Locate and identify every blood parasite.
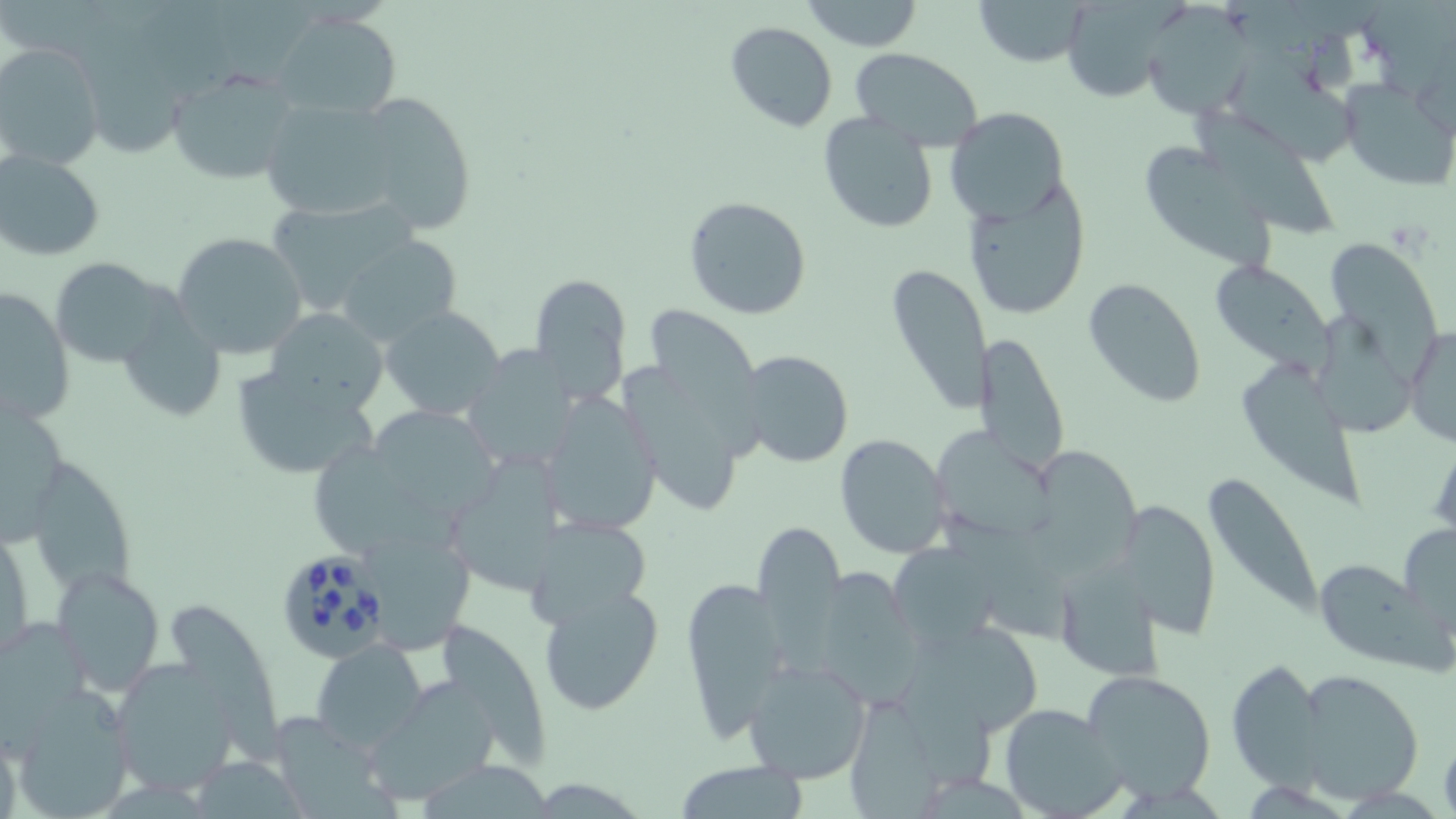
Approximate bounding boxes as (x1, y1, x2, y2) in pixels.
Babesia divergens-infected red blood cells: (281, 545, 401, 661).
No Plasmodium falciparum, Plasmodium ovale, Plasmodium malariae, Plasmodium vivax, or Trypanosoma brucei observed.

Uninfected red blood cell locations: (802, 0, 923, 52), (972, 0, 1090, 68), (1056, 0, 1181, 104), (1142, 10, 1245, 118), (272, 12, 401, 120), (724, 21, 839, 133), (0, 41, 106, 169), (848, 48, 985, 152), (1223, 54, 1359, 172), (167, 70, 301, 188), (1341, 82, 1452, 187), (352, 92, 478, 235), (259, 97, 403, 219), (946, 107, 1068, 225), (818, 111, 938, 233), (1194, 111, 1343, 242), (1145, 146, 1277, 277), (0, 148, 104, 260), (962, 181, 1094, 319), (684, 195, 814, 321), (172, 231, 309, 358), (334, 234, 463, 345), (1326, 241, 1444, 390), (49, 258, 181, 369), (1207, 260, 1332, 371), (884, 261, 994, 415), (529, 273, 633, 405), (1083, 277, 1207, 408), (126, 279, 226, 423), (1, 285, 75, 426), (645, 305, 764, 410), (380, 306, 507, 419), (261, 307, 389, 420), (1316, 317, 1421, 449), (1404, 323, 1456, 447), (977, 332, 1070, 476), (459, 347, 586, 472), (735, 349, 855, 468), (617, 359, 754, 520), (1243, 362, 1365, 512), (228, 364, 378, 480), (539, 390, 662, 535), (0, 401, 67, 562), (368, 412, 515, 534), (930, 429, 1069, 544), (833, 433, 953, 559), (312, 437, 434, 558), (1025, 447, 1156, 583), (447, 452, 567, 595), (40, 464, 142, 617), (1198, 469, 1324, 620), (1116, 497, 1221, 639), (523, 514, 657, 635), (753, 520, 848, 663), (1399, 520, 1456, 634), (367, 530, 481, 655), (887, 542, 999, 653), (1049, 555, 1166, 677), (1310, 562, 1437, 668), (53, 566, 165, 697), (818, 568, 945, 716), (676, 572, 787, 740), (537, 585, 665, 717), (167, 603, 289, 778), (430, 616, 555, 768), (907, 617, 1046, 737), (0, 619, 94, 740), (312, 639, 427, 751), (1226, 656, 1328, 791), (743, 659, 873, 785), (108, 661, 239, 797), (1293, 667, 1424, 804), (1081, 668, 1218, 800), (358, 678, 501, 806), (9, 686, 136, 817), (838, 691, 964, 816), (996, 702, 1128, 819), (268, 712, 398, 819), (1440, 733, 1456, 819), (184, 757, 312, 816), (413, 760, 558, 816), (673, 761, 810, 817). Slide-level diagnosis: Babesia divergens. Light microscopy. Captured at 1000x magnification. Image is 1456×819 pixels. Single field of view. May-Grünwald-Giemsa stain. Thin blood smear.